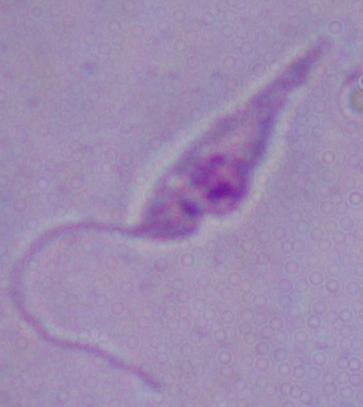
Micrograph. A Leishmania parasite is seen. 1000x magnification.